State which parasite is depicted.
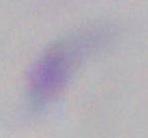

Toxoplasma gondii.

Captured at 1000x magnification. Micrograph.